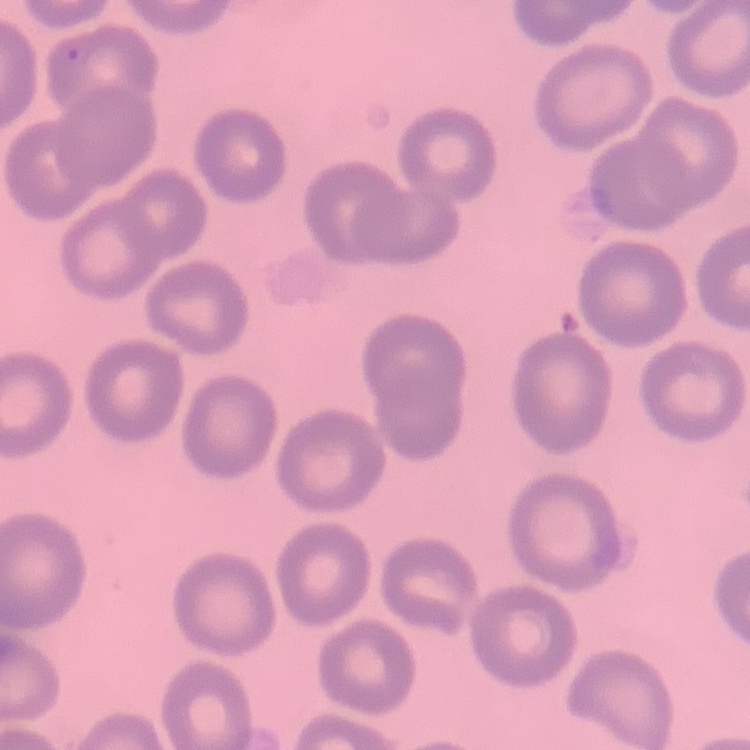 The red blood cells exhibit no rouleaux formation. One tile cut from a larger photomicrograph. Thin peripheral smear. Field's or Giemsa stain.